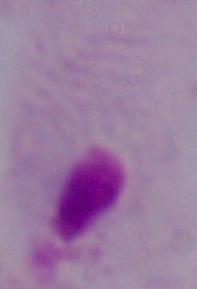
identification = trichomonad
magnification = 1000x
modality = photomicrograph